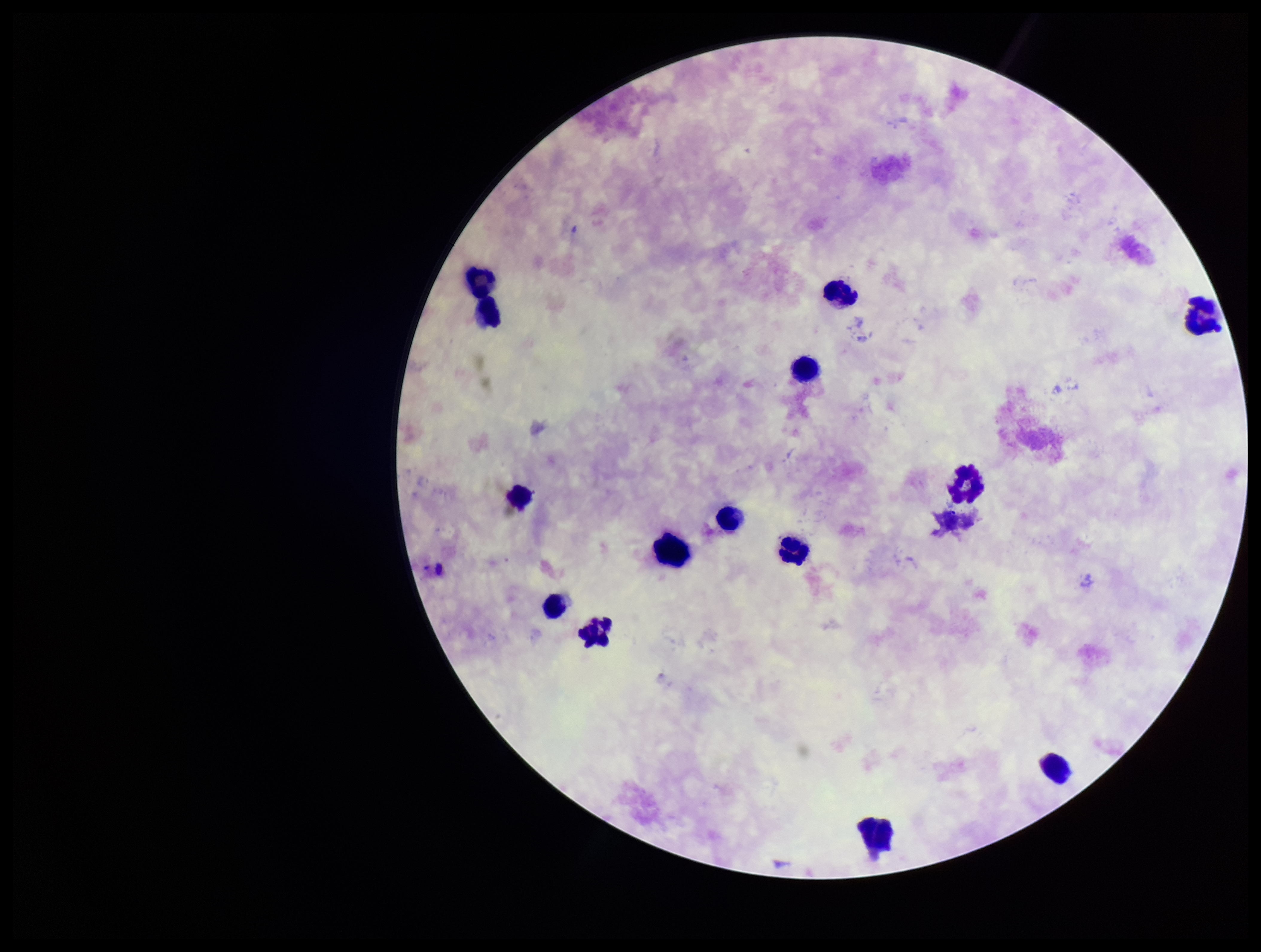

Summary:
  - Leukocyte count: 14
  - Capture: smartphone photograph through the microscope eyepiece
  - Plasmodium parasites: none identified
  - Stain: Giemsa
  - Field of view: single
  - Patient malaria status: negative
  - Image size: 1261×952 pixels
  - Preparation: thick
  - Parasite count: 0